Locate and identify every blood parasite.
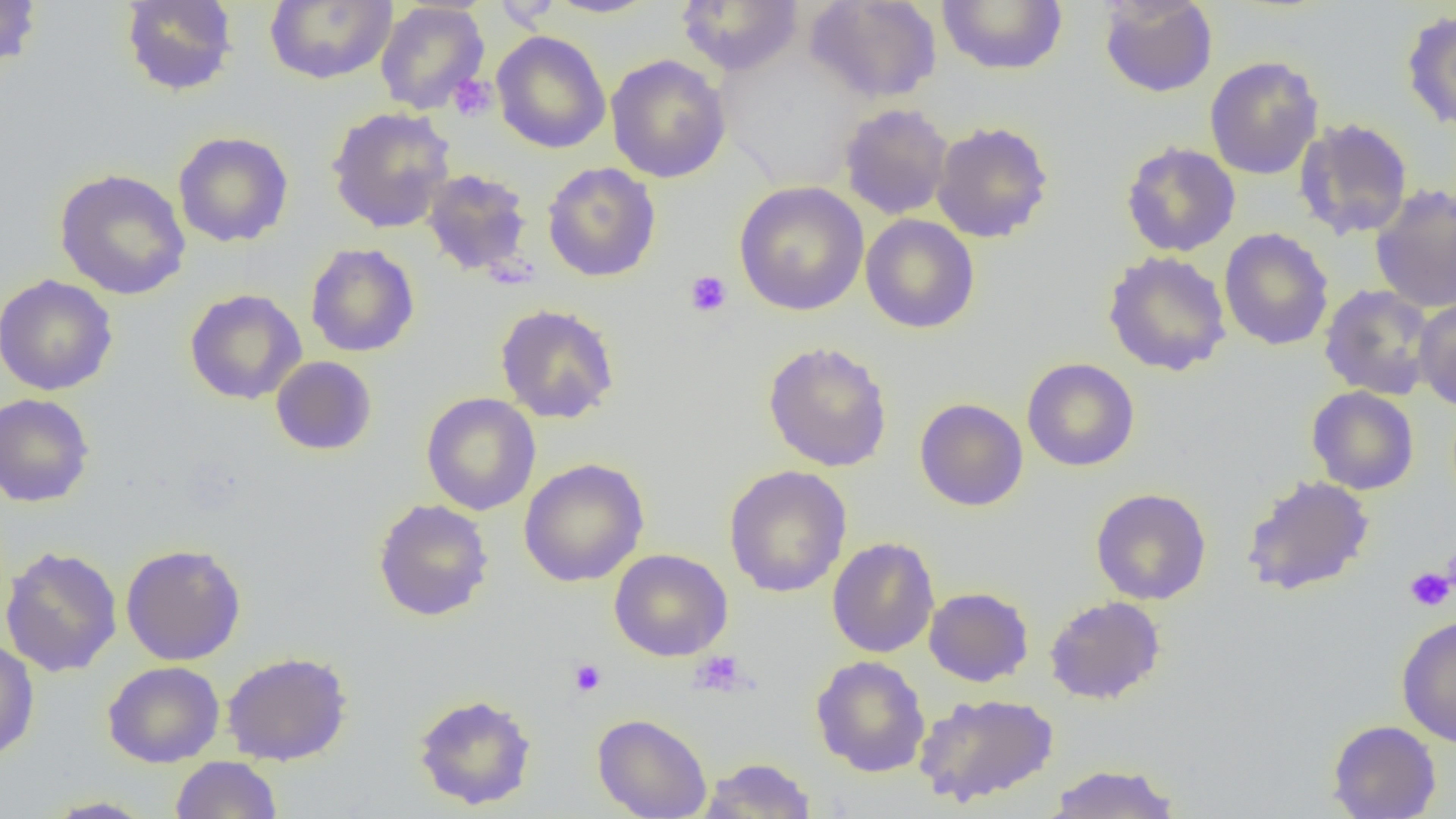
No blood parasites seen.

Approximate bounding boxes as named x1/y1/x2/y2 corners in pixels. Uninfected red blood cell locations: (x1=0, y1=0, x2=42, y2=72), (x1=264, y1=0, x2=397, y2=85), (x1=544, y1=0, x2=660, y2=18), (x1=804, y1=0, x2=942, y2=104), (x1=936, y1=0, x2=1068, y2=75), (x1=1099, y1=0, x2=1218, y2=98), (x1=120, y1=1, x2=238, y2=97), (x1=375, y1=1, x2=490, y2=115), (x1=676, y1=1, x2=804, y2=76), (x1=1401, y1=10, x2=1456, y2=132), (x1=491, y1=31, x2=611, y2=154), (x1=605, y1=54, x2=731, y2=184), (x1=1204, y1=55, x2=1324, y2=180), (x1=839, y1=103, x2=954, y2=220), (x1=326, y1=107, x2=456, y2=233), (x1=1294, y1=118, x2=1414, y2=241), (x1=931, y1=121, x2=1054, y2=243), (x1=173, y1=131, x2=294, y2=248), (x1=1120, y1=141, x2=1241, y2=257), (x1=542, y1=161, x2=661, y2=282), (x1=54, y1=168, x2=192, y2=301), (x1=421, y1=168, x2=533, y2=276), (x1=734, y1=181, x2=869, y2=316), (x1=1370, y1=184, x2=1456, y2=314), (x1=860, y1=214, x2=980, y2=334), (x1=1219, y1=228, x2=1334, y2=351), (x1=306, y1=243, x2=419, y2=357), (x1=1102, y1=251, x2=1232, y2=377), (x1=0, y1=274, x2=118, y2=396), (x1=1319, y1=284, x2=1437, y2=400), (x1=184, y1=288, x2=307, y2=405), (x1=1414, y1=298, x2=1456, y2=411), (x1=495, y1=303, x2=620, y2=424), (x1=763, y1=341, x2=892, y2=472), (x1=270, y1=356, x2=377, y2=456), (x1=1022, y1=358, x2=1139, y2=472), (x1=1306, y1=386, x2=1419, y2=495), (x1=421, y1=392, x2=541, y2=516), (x1=0, y1=393, x2=95, y2=508), (x1=914, y1=397, x2=1028, y2=511), (x1=518, y1=458, x2=649, y2=587), (x1=723, y1=465, x2=852, y2=598), (x1=1240, y1=474, x2=1375, y2=596), (x1=1090, y1=487, x2=1212, y2=605), (x1=372, y1=498, x2=494, y2=622), (x1=826, y1=537, x2=940, y2=658), (x1=120, y1=543, x2=247, y2=666), (x1=0, y1=545, x2=123, y2=677), (x1=608, y1=549, x2=733, y2=662), (x1=924, y1=586, x2=1034, y2=686), (x1=1044, y1=595, x2=1166, y2=705), (x1=1396, y1=615, x2=1456, y2=748), (x1=0, y1=637, x2=39, y2=761), (x1=222, y1=650, x2=353, y2=766), (x1=811, y1=655, x2=931, y2=778), (x1=103, y1=660, x2=225, y2=767), (x1=412, y1=692, x2=538, y2=811), (x1=914, y1=692, x2=1059, y2=807), (x1=592, y1=713, x2=712, y2=819), (x1=1327, y1=719, x2=1441, y2=818), (x1=170, y1=756, x2=282, y2=818), (x1=698, y1=757, x2=818, y2=818), (x1=1044, y1=762, x2=1182, y2=818), (x1=40, y1=796, x2=157, y2=818). Platelet locations: (x1=448, y1=74, x2=497, y2=122), (x1=685, y1=270, x2=732, y2=317), (x1=1405, y1=566, x2=1455, y2=612), (x1=690, y1=650, x2=750, y2=697), (x1=568, y1=658, x2=607, y2=697). Slide-level diagnosis: negative for blood parasites. Optical microscopy. Image is 1456×819 pixels. 1000x magnification. One field of a larger specimen. Thin blood film.